Identify the parasite.
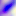

This is Toxoplasma gondii.

Micrograph. 400x magnification.